Identify the parasite.
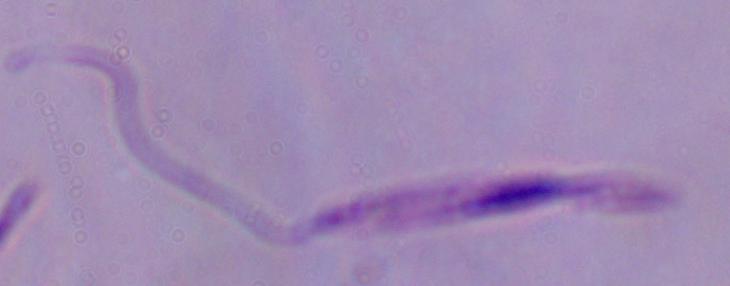

This is Leishmania.

modality = photomicrograph
magnification = 1000x